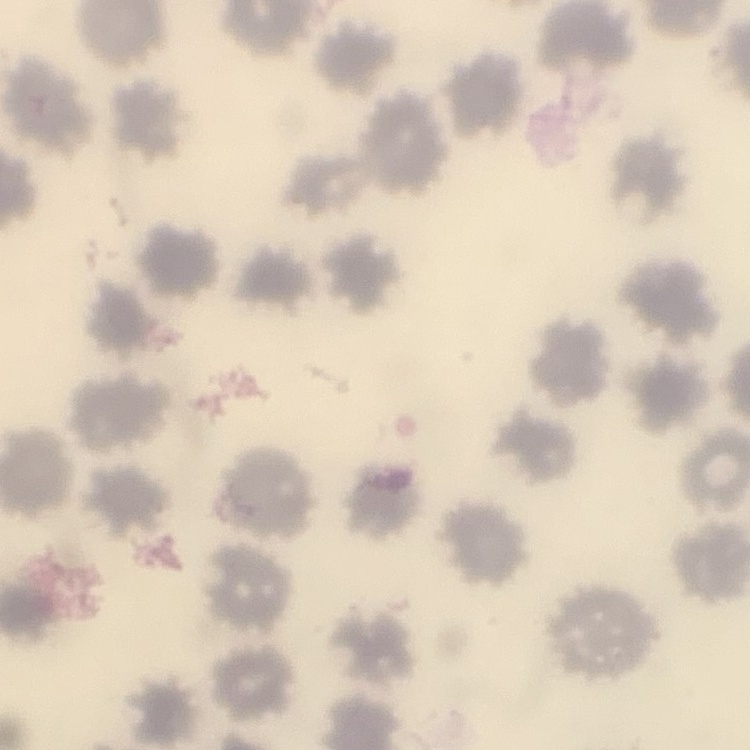
{
  "red_blood_cell_morphology": "no rouleaux formation",
  "stain": "Field's or Giemsa",
  "image_type": "square crop of a larger photomicrograph",
  "preparation": "thin blood smear"
}